State which parasite is depicted.
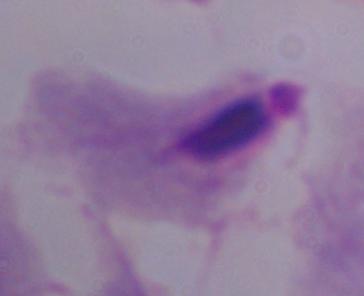

This is a trichomonad.

Summary:
  - Modality: micrograph
  - Magnification: 1000x